Identify the blood parasite species.
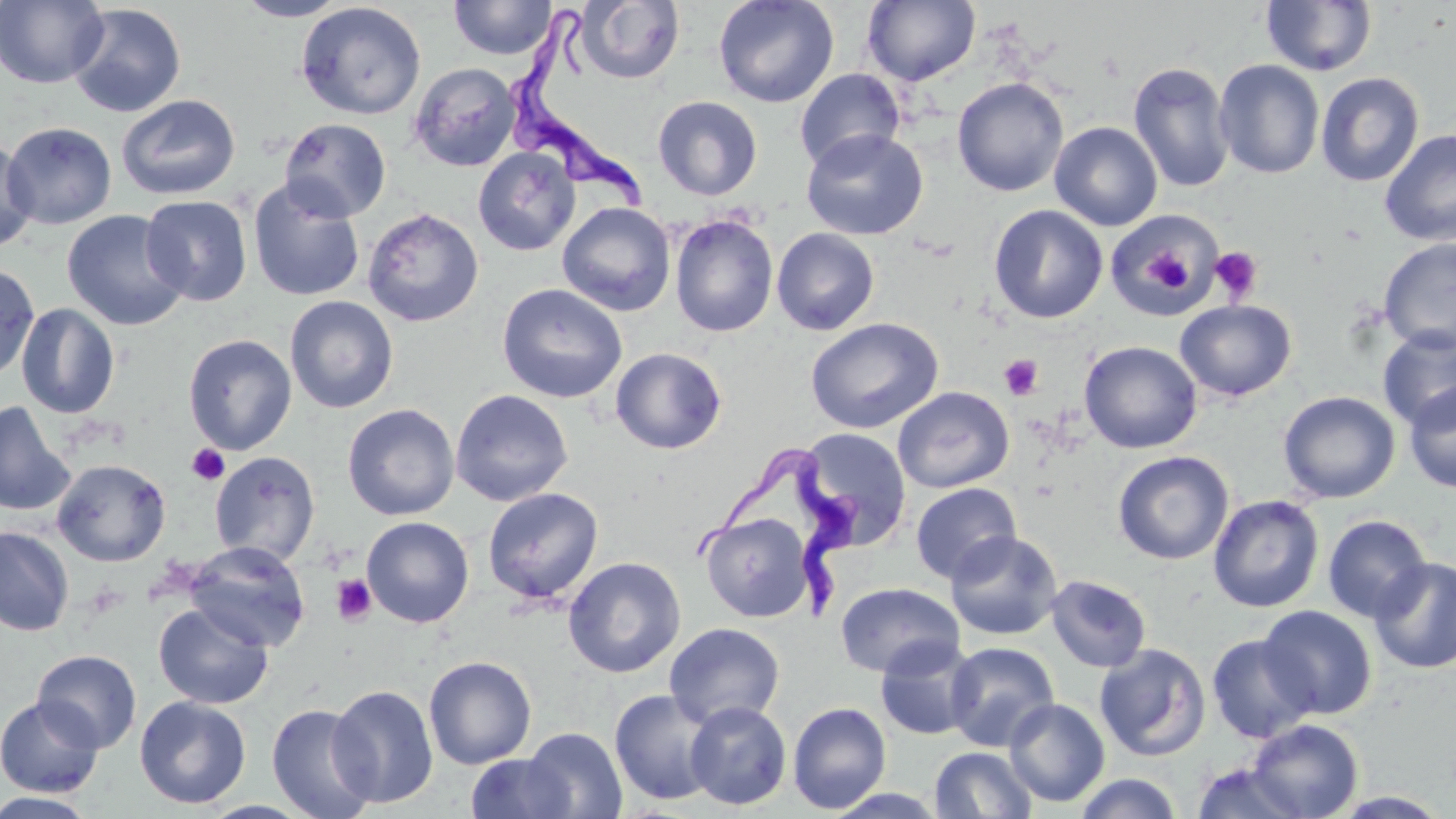

Trypanosoma brucei.

magnification: 1000x
modality: optical microscopy
image_size: 1456×819 pixels
field_of_view: one of a larger specimen
stain: May-Grünwald-Giemsa
trypanosoma_brucei_locations: 'approximate bounding boxes as named x1/y1/x2/y2 corners in pixels: (x1=509, y1=2, x2=654, y2=210), (x1=690, y1=440, x2=858, y2=621)'
platelet_locations: 'approximate bounding boxes as named x1/y1/x2/y2 corners in pixels: (x1=1136, y1=241, x2=1195, y2=294), (x1=1210, y1=246, x2=1263, y2=303), (x1=999, y1=354, x2=1044, y2=400), (x1=187, y1=443, x2=230, y2=486), (x1=330, y1=574, x2=377, y2=626)'
preparation: thin blood smear
uninfected_red_blood_cell_locations: 'approximate bounding boxes as named x1/y1/x2/y2 corners in pixels: (x1=0, y1=0, x2=109, y2=89), (x1=233, y1=0, x2=351, y2=21), (x1=448, y1=0, x2=557, y2=60), (x1=713, y1=0, x2=839, y2=109), (x1=575, y1=1, x2=685, y2=84), (x1=862, y1=1, x2=981, y2=86), (x1=1261, y1=1, x2=1378, y2=77), (x1=296, y1=2, x2=426, y2=120), (x1=67, y1=3, x2=187, y2=117), (x1=1214, y1=60, x2=1325, y2=179), (x1=1128, y1=61, x2=1235, y2=193), (x1=408, y1=62, x2=521, y2=172), (x1=794, y1=68, x2=905, y2=173), (x1=1315, y1=71, x2=1424, y2=187), (x1=952, y1=77, x2=1068, y2=197), (x1=116, y1=94, x2=241, y2=200), (x1=653, y1=95, x2=763, y2=201), (x1=278, y1=117, x2=392, y2=222), (x1=1049, y1=121, x2=1163, y2=231), (x1=2, y1=122, x2=117, y2=229), (x1=801, y1=128, x2=927, y2=240), (x1=1379, y1=128, x2=1456, y2=246), (x1=0, y1=138, x2=38, y2=251), (x1=473, y1=147, x2=581, y2=256), (x1=247, y1=178, x2=365, y2=302), (x1=140, y1=194, x2=253, y2=306), (x1=557, y1=202, x2=676, y2=316), (x1=989, y1=204, x2=1107, y2=324), (x1=362, y1=207, x2=484, y2=327), (x1=61, y1=209, x2=190, y2=330), (x1=1106, y1=212, x2=1223, y2=319), (x1=669, y1=214, x2=778, y2=337), (x1=771, y1=228, x2=879, y2=335), (x1=1378, y1=237, x2=1456, y2=353), (x1=0, y1=262, x2=40, y2=381), (x1=496, y1=283, x2=627, y2=403), (x1=284, y1=295, x2=399, y2=414), (x1=1174, y1=299, x2=1297, y2=402), (x1=15, y1=303, x2=121, y2=419), (x1=805, y1=317, x2=944, y2=434), (x1=1377, y1=326, x2=1456, y2=431), (x1=183, y1=333, x2=297, y2=455), (x1=1079, y1=340, x2=1202, y2=453), (x1=610, y1=347, x2=727, y2=454), (x1=1404, y1=382, x2=1456, y2=493), (x1=893, y1=386, x2=1014, y2=493), (x1=450, y1=388, x2=573, y2=507), (x1=1278, y1=390, x2=1400, y2=503), (x1=0, y1=400, x2=75, y2=516), (x1=342, y1=403, x2=460, y2=521), (x1=797, y1=428, x2=911, y2=548), (x1=1112, y1=450, x2=1234, y2=564), (x1=209, y1=451, x2=321, y2=566), (x1=52, y1=458, x2=171, y2=567), (x1=910, y1=483, x2=1022, y2=584), (x1=482, y1=487, x2=604, y2=605), (x1=1208, y1=494, x2=1324, y2=613), (x1=700, y1=512, x2=815, y2=622), (x1=1323, y1=515, x2=1432, y2=623), (x1=360, y1=516, x2=475, y2=627), (x1=0, y1=526, x2=74, y2=636), (x1=945, y1=530, x2=1063, y2=640), (x1=184, y1=540, x2=311, y2=651), (x1=563, y1=556, x2=686, y2=678), (x1=1369, y1=557, x2=1456, y2=673), (x1=1046, y1=575, x2=1152, y2=673), (x1=835, y1=582, x2=964, y2=678), (x1=153, y1=602, x2=274, y2=709), (x1=1258, y1=605, x2=1377, y2=719), (x1=664, y1=622, x2=785, y2=730), (x1=1206, y1=633, x2=1318, y2=743), (x1=875, y1=638, x2=980, y2=741), (x1=944, y1=641, x2=1059, y2=752), (x1=1094, y1=643, x2=1211, y2=761), (x1=32, y1=649, x2=142, y2=753), (x1=424, y1=656, x2=537, y2=769), (x1=328, y1=684, x2=439, y2=808), (x1=609, y1=688, x2=721, y2=807), (x1=0, y1=695, x2=104, y2=798), (x1=134, y1=695, x2=251, y2=808), (x1=1004, y1=698, x2=1110, y2=806), (x1=684, y1=701, x2=792, y2=810), (x1=787, y1=701, x2=892, y2=814), (x1=266, y1=703, x2=378, y2=819), (x1=1245, y1=718, x2=1364, y2=818), (x1=522, y1=727, x2=627, y2=818), (x1=930, y1=747, x2=1037, y2=819), (x1=465, y1=753, x2=577, y2=818), (x1=1190, y1=760, x2=1310, y2=818), (x1=1073, y1=772, x2=1184, y2=819), (x1=821, y1=787, x2=950, y2=818), (x1=0, y1=791, x2=101, y2=818), (x1=1331, y1=791, x2=1453, y2=817)'